Identify the parasite.
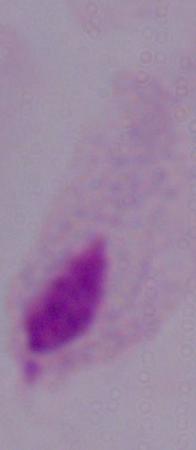
This is a trichomonad.

modality = photomicrograph
magnification = 1000x